Name the parasite shown.
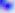
Toxoplasma gondii.

modality = photomicrograph
magnification = 400x